Report the malaria status of this cell.
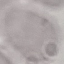
It is uninfected.

Cell patch, automatically extracted from a larger field of view and resized to 64 × 64 pixels. Giemsa-stained preparation. Thin blood smear. Acquired by smartphone through the microscope eyepiece.